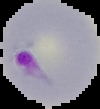 Malaria status: parasitized. Image is 100×109 pixels. From a thin blood smear. Segmented cell region on a black background.